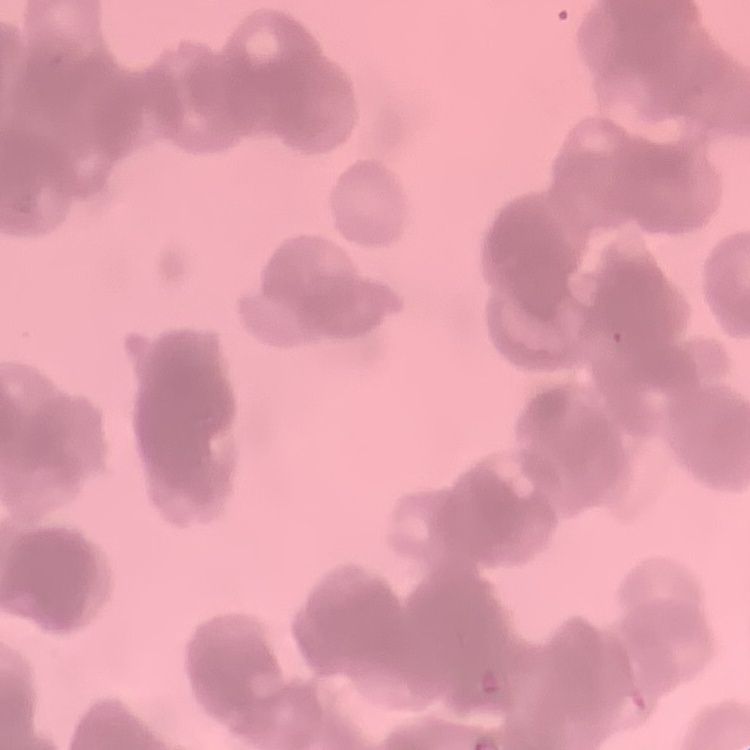

The erythrocytes show rouleaux formation. Field's or Giemsa stain. One tile cut from a larger photomicrograph. Thin peripheral smear.